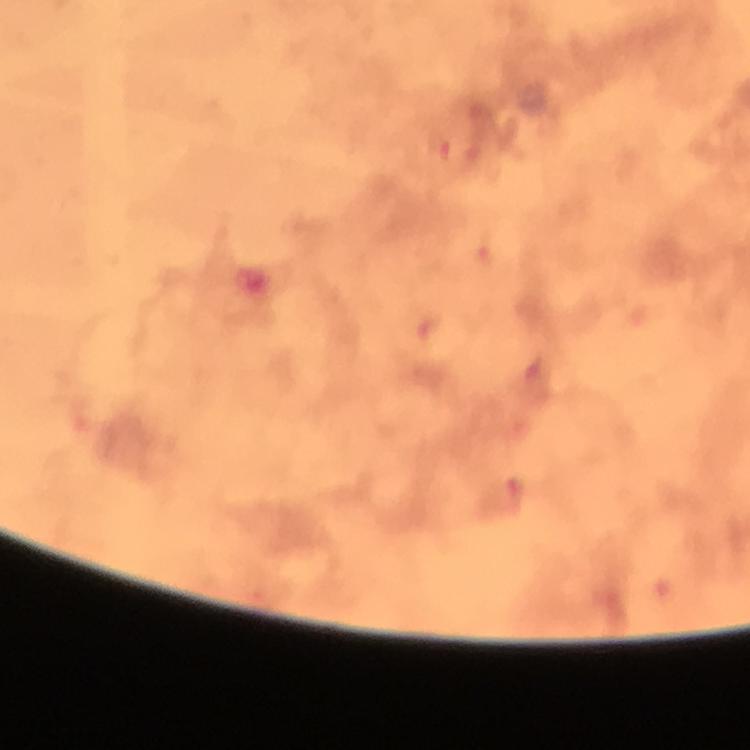 Approximate centers as (x, y) in pixels. Malaria parasite locations: (437, 149), (482, 256), (424, 330). Photographed through the microscope with a smartphone camera. Cropped region of a single field of view. Thick smear. From a malaria diagnostic workup. Image is 750×750 pixels. Immersion oil applied. 100x magnification. Giemsa stain.